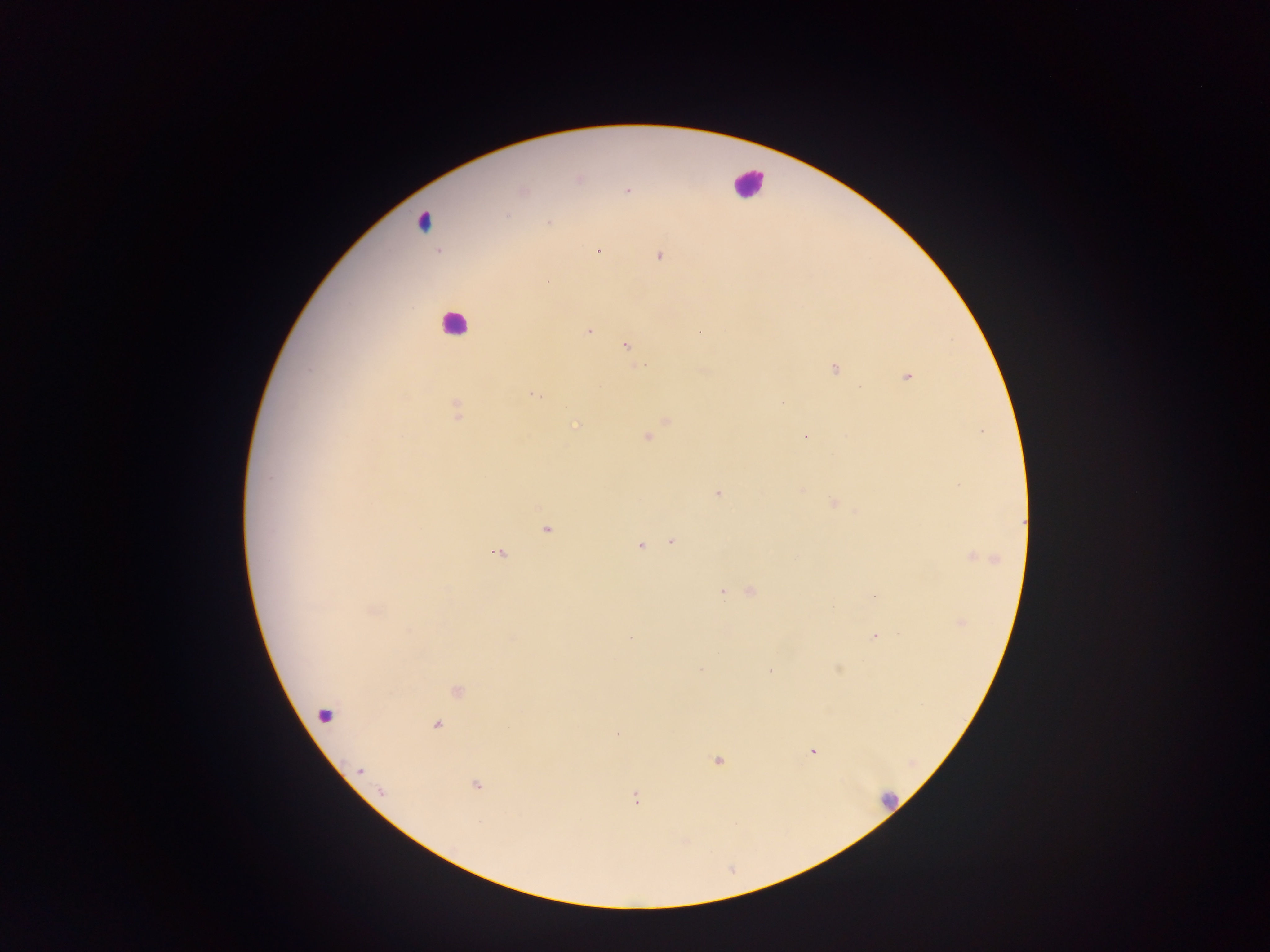
Approximate centers as (x, y) in pixels. Plasmodium parasite locations: (579, 179), (524, 190), (627, 191), (507, 215), (548, 223), (599, 251), (659, 256), (547, 283), (589, 331), (626, 345), (835, 368), (309, 370), (906, 376), (534, 396), (457, 410), (576, 426), (805, 437), (647, 439), (269, 478), (960, 485), (717, 494), (833, 503), (546, 529), (671, 541), (639, 545), (499, 554), (980, 558), (722, 592), (751, 592), (873, 595), (374, 612), (962, 622), (874, 636), (631, 637), (700, 669), (838, 669), (769, 671), (458, 691), (437, 724), (617, 733), (812, 752), (718, 761), (360, 771), (476, 786), (636, 799). Leukocyte locations (subset; some below the resolvable size): (747, 183), (422, 223), (455, 323), (324, 716), (887, 799). Sample from Ghana. Image is 1270×952 pixels. One field of view. Thick blood film. Mobile-phone photograph taken through the microscope.